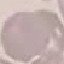 Malaria status: uninfected. Acquired by smartphone through the microscope eyepiece. Automatically extracted cell patch, resized to 64 × 64 pixels. Thin smear of blood. Giemsa-stained preparation.